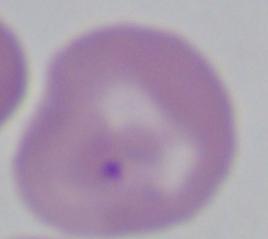

1000x magnification. A Babesia parasite is seen. Micrograph.